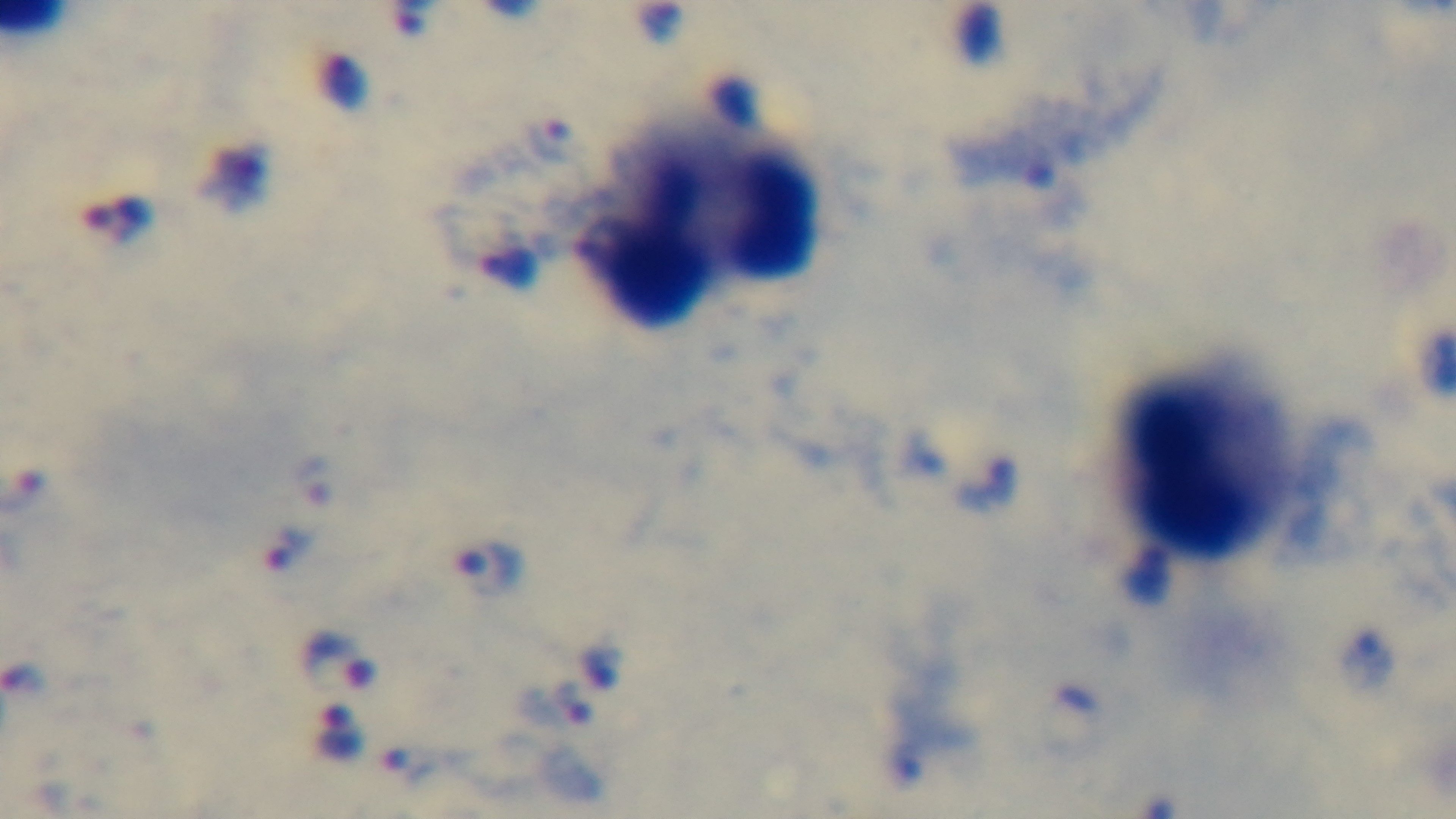
{
  "capture": "mounted 4K digital camera",
  "malaria_status": "infected",
  "field_of_view": "one from the slide",
  "stain": "Giemsa",
  "objective": "100x oil immersion",
  "preparation": "thick",
  "modality": "light microscopy"
}